Locate every Plasmodium parasite and every leukocyte.
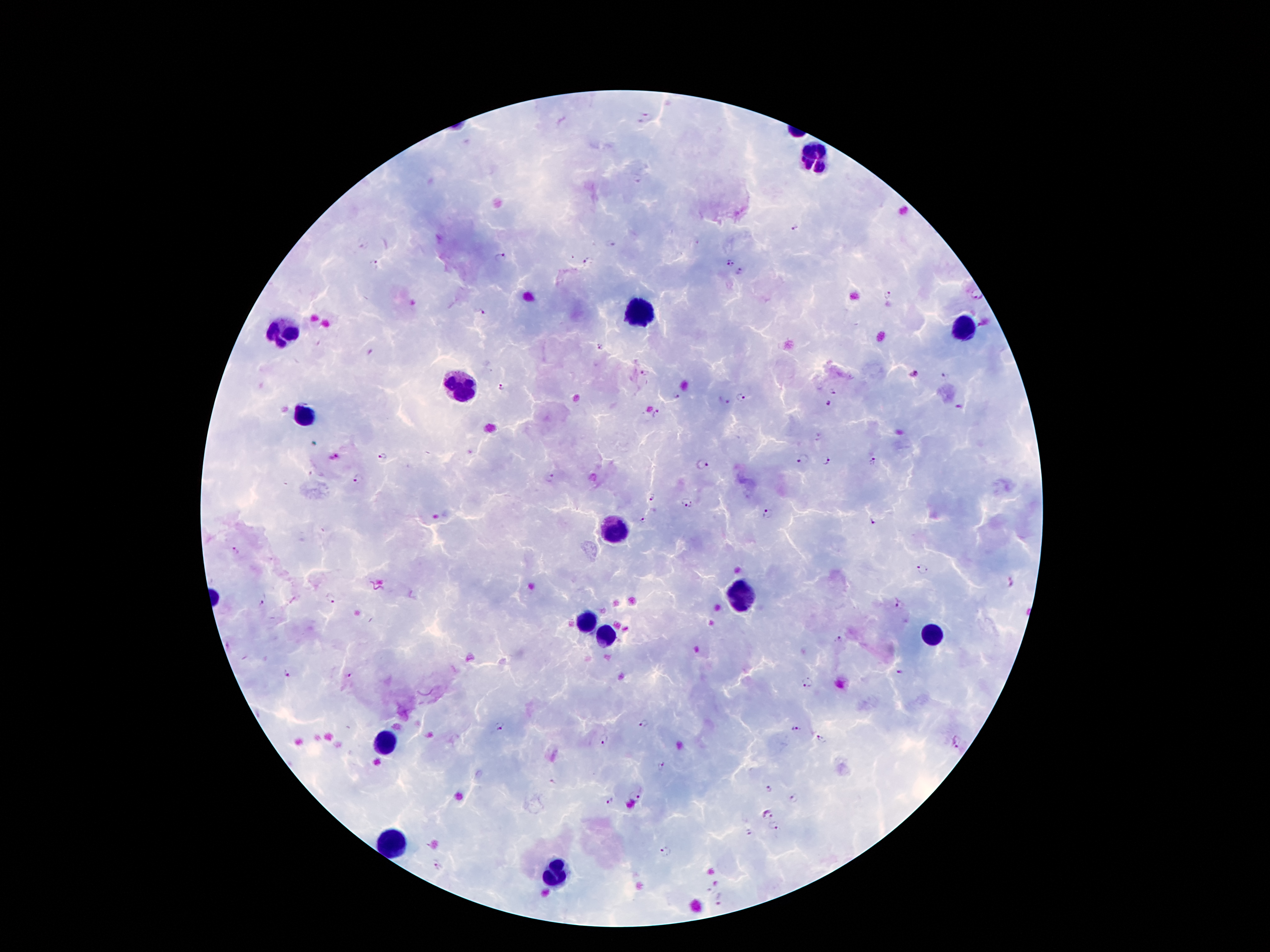
Approximate object centers, in pixels from the top-left corner.
Plasmodium parasites: (x=646, y=117), (x=796, y=226), (x=610, y=244), (x=499, y=256), (x=588, y=262), (x=374, y=263), (x=730, y=264), (x=739, y=272), (x=975, y=294), (x=888, y=295), (x=486, y=311), (x=601, y=346), (x=646, y=373), (x=915, y=376), (x=945, y=376), (x=502, y=386), (x=834, y=391), (x=676, y=396), (x=741, y=398), (x=828, y=405), (x=958, y=407), (x=656, y=414), (x=334, y=457), (x=383, y=457), (x=803, y=461), (x=826, y=462), (x=873, y=462), (x=701, y=465), (x=551, y=478), (x=360, y=479), (x=651, y=498), (x=687, y=503), (x=770, y=513), (x=873, y=520), (x=642, y=521), (x=235, y=552), (x=924, y=570), (x=1011, y=584), (x=330, y=600), (x=263, y=604), (x=896, y=605), (x=840, y=640), (x=897, y=672), (x=287, y=675), (x=349, y=675), (x=805, y=682), (x=643, y=724), (x=499, y=726), (x=796, y=729), (x=605, y=739), (x=822, y=741), (x=957, y=742), (x=662, y=765), (x=771, y=788), (x=634, y=799), (x=794, y=799), (x=610, y=802), (x=765, y=813), (x=774, y=827), (x=665, y=851), (x=437, y=866), (x=721, y=901).
Leukocytes: (x=814, y=152), (x=639, y=313), (x=964, y=329), (x=283, y=332), (x=464, y=386), (x=305, y=415), (x=615, y=529), (x=743, y=595), (x=586, y=620), (x=608, y=636), (x=933, y=636), (x=383, y=740), (x=389, y=844), (x=551, y=875).

preparation: thick blood smear
patient_malaria_status: infected with Plasmodium falciparum
field_of_view: single
capture: smartphone through the microscope eyepiece
image_size: 1270×952 pixels
magnification: 100x
stain: Giemsa